Identify the blood parasite species.
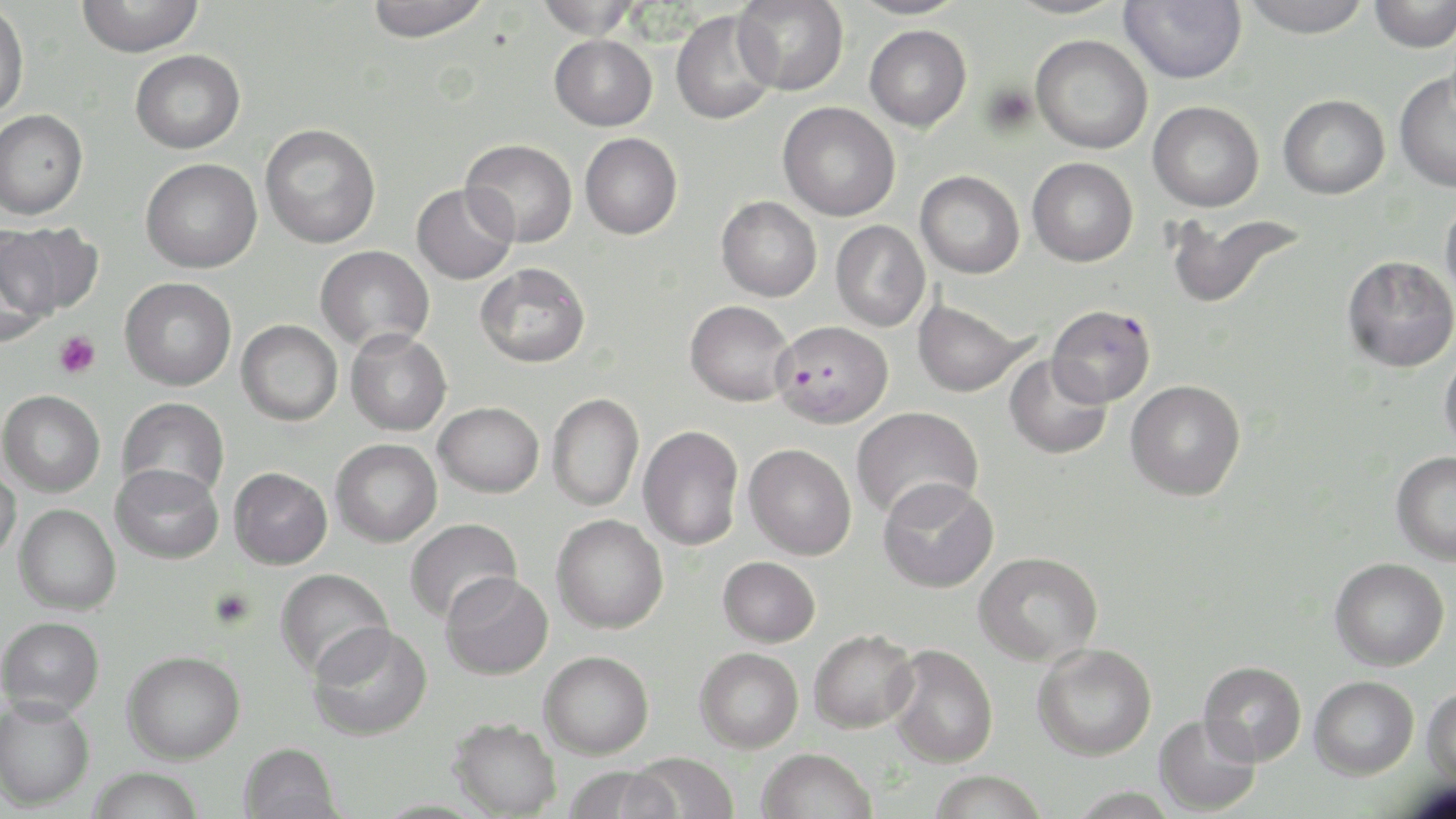

Plasmodium falciparum.

Approximate bounding boxes as [x1, y1, x2, y2] in pixels. Uninfected red blood cell locations: [76, 0, 204, 57], [364, 0, 491, 43], [534, 0, 642, 39], [734, 0, 849, 95], [848, 0, 971, 20], [1004, 0, 1128, 19], [1120, 0, 1246, 84], [1240, 0, 1372, 38], [1368, 0, 1456, 53], [0, 2, 30, 122], [670, 10, 779, 125], [864, 24, 972, 132], [550, 34, 657, 131], [1030, 34, 1153, 154], [130, 49, 245, 154], [1394, 71, 1456, 193], [1278, 94, 1390, 199], [1148, 100, 1264, 212], [778, 102, 900, 221], [0, 108, 88, 220], [259, 123, 381, 249], [580, 132, 683, 239], [460, 138, 578, 248], [1027, 157, 1138, 267], [141, 158, 262, 273], [915, 170, 1024, 278], [411, 183, 518, 284], [1441, 193, 1456, 304], [716, 196, 822, 302], [1165, 210, 1307, 311], [831, 220, 930, 332], [2, 221, 104, 316], [0, 230, 59, 345], [315, 245, 435, 352], [1342, 255, 1456, 373], [475, 262, 591, 368], [119, 277, 236, 390], [913, 298, 1033, 398], [685, 300, 795, 406], [237, 320, 342, 426], [345, 329, 452, 436], [1439, 349, 1456, 454], [1004, 354, 1112, 460], [1125, 379, 1246, 500], [0, 390, 105, 497], [546, 393, 644, 511], [117, 397, 229, 499], [434, 402, 544, 497], [851, 407, 982, 522], [638, 426, 743, 550], [331, 439, 442, 547], [744, 443, 857, 560], [1391, 451, 1456, 565], [0, 463, 22, 563], [110, 463, 223, 564], [229, 467, 332, 569], [877, 477, 999, 593], [14, 504, 121, 615], [551, 514, 668, 633], [404, 518, 522, 624], [974, 551, 1103, 666], [718, 556, 820, 647], [1330, 557, 1449, 670], [275, 567, 394, 680], [441, 572, 553, 680], [1, 615, 105, 718], [307, 621, 432, 741], [809, 629, 919, 733], [1032, 642, 1157, 761], [887, 644, 999, 768], [695, 647, 804, 753], [122, 650, 245, 764], [539, 650, 654, 759], [1199, 661, 1307, 766], [1309, 675, 1419, 779], [1422, 686, 1456, 788], [0, 696, 95, 811], [1154, 714, 1260, 816], [448, 717, 561, 818], [239, 742, 342, 819], [757, 748, 877, 819], [626, 752, 740, 819], [562, 765, 679, 819], [87, 767, 205, 819], [928, 770, 1048, 819]. Platelet locations: [54, 331, 101, 379]. Plasmodium falciparum-infected red blood cell locations: [1046, 304, 1156, 406], [772, 319, 893, 427]. Optical microscopy. One field of a larger specimen. Image is 1456×819 pixels. Thin blood smear. May-Grünwald-Giemsa stain. 1000x magnification.